Assess the morphology of the erythrocytes.
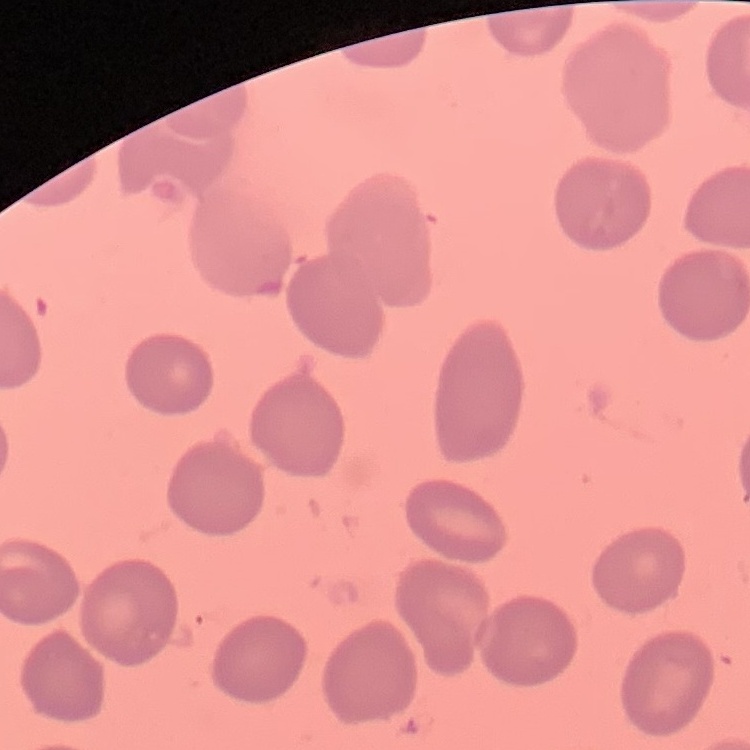
No rouleaux formation.

{
  "stain": "Field's or Giemsa",
  "image_type": "one tile cut from a larger photomicrograph",
  "preparation": "thin blood smear"
}